Rate the background quality.
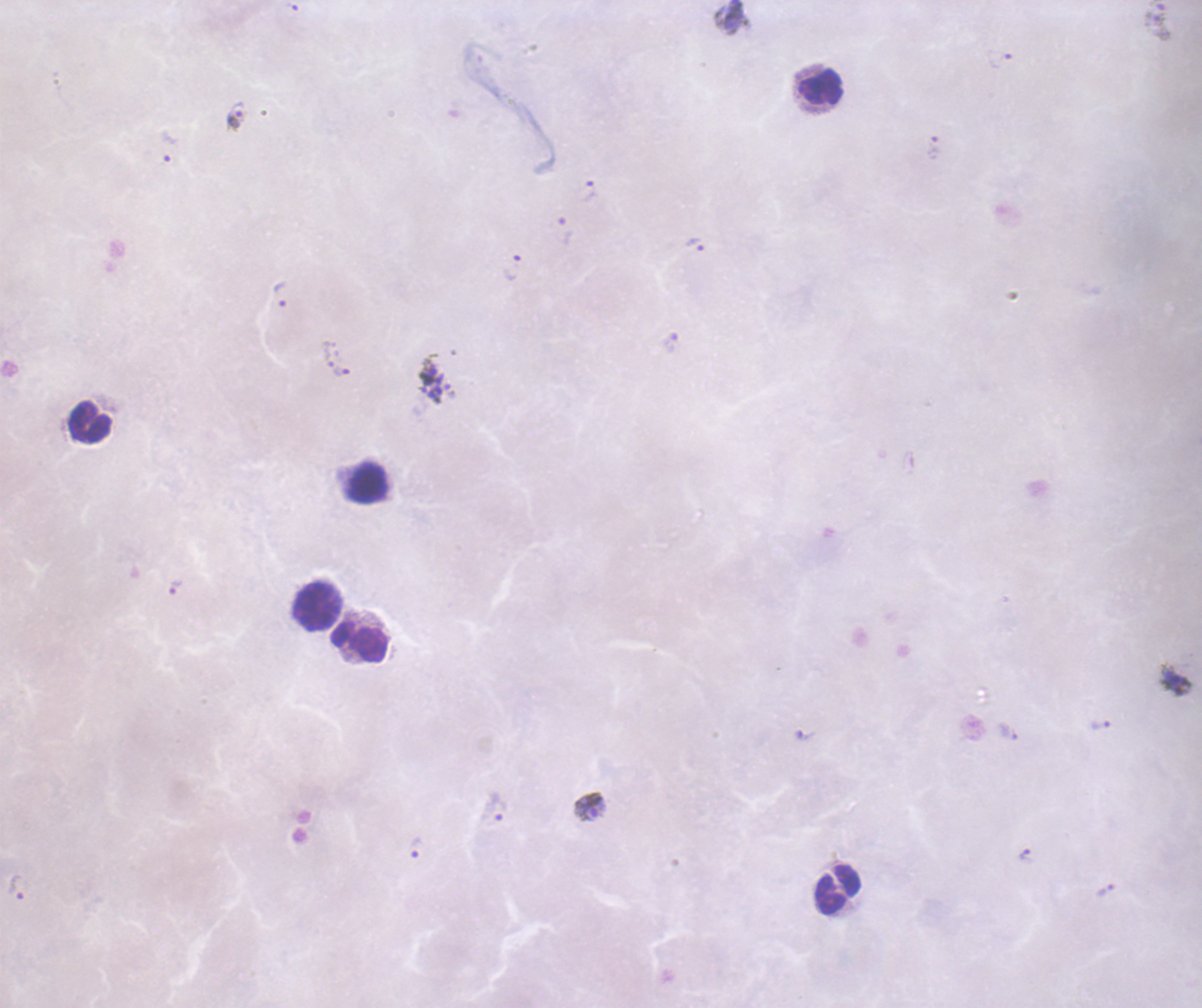
Poor.

{
  "life_cycle_stages_observed": "trophozoite, schizont",
  "coloration_quality": "bad",
  "context": "previously used in a real diagnosis",
  "leukocyte_locations": "approximate centers as {x, y} in pixels: {822, 87}, {91, 423}, {368, 483}, {318, 607}, {359, 643}, {840, 892}",
  "preparation": "thick smear of blood",
  "result": "Plasmodium parasites identified",
  "schizont_locations": "approximate centers as {x, y} in pixels: {434, 380}",
  "image_size": "1202×1008 pixels",
  "trophozoite_locations": "approximate centers as {x, y} in pixels: {235, 115}, {169, 147}, {933, 147}, {588, 192}, {565, 230}, {695, 245}, {513, 268}, {281, 293}, {329, 354}, {342, 372}, {175, 588}, {1101, 724}, {496, 807}, {590, 807}, {415, 847}, {1026, 856}, {17, 888}",
  "stain": "Romanowsky",
  "magnification": "100x",
  "field_of_view": "single"
}